Assess this cell for malaria.
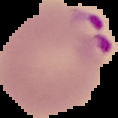

It is parasitized.

Summary:
  - Image type: segmented cell region with the area outside set to black
  - Image size: 118×118 pixels
  - Preparation: thin blood film